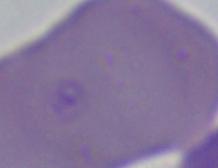

Summary:
  - Magnification: 1000x
  - Modality: photomicrograph
  - Identification: Babesia